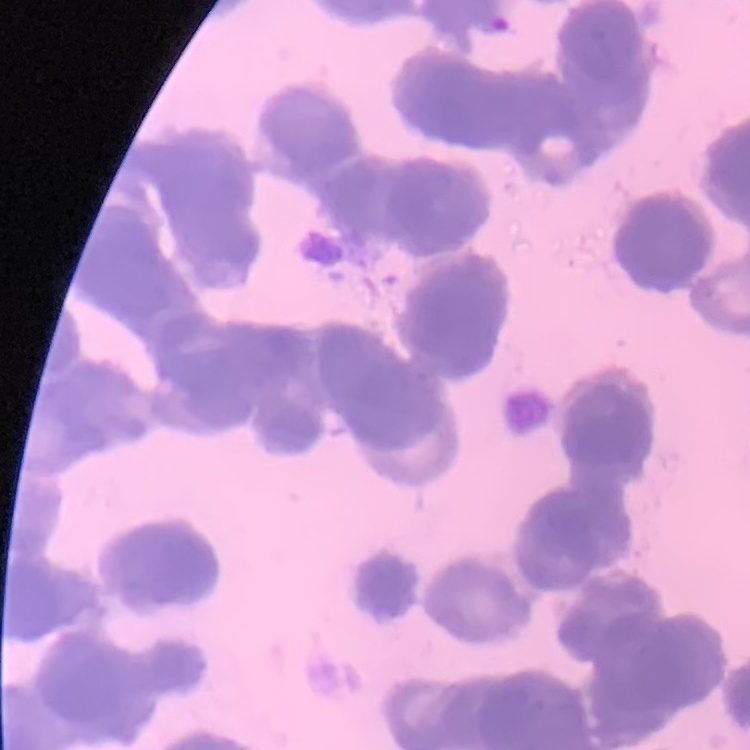

Summary:
  - Erythrocyte morphology: rouleaux formation
  - Stain: Field's or Giemsa
  - Image type: square crop of a larger photomicrograph
  - Preparation: thin peripheral smear